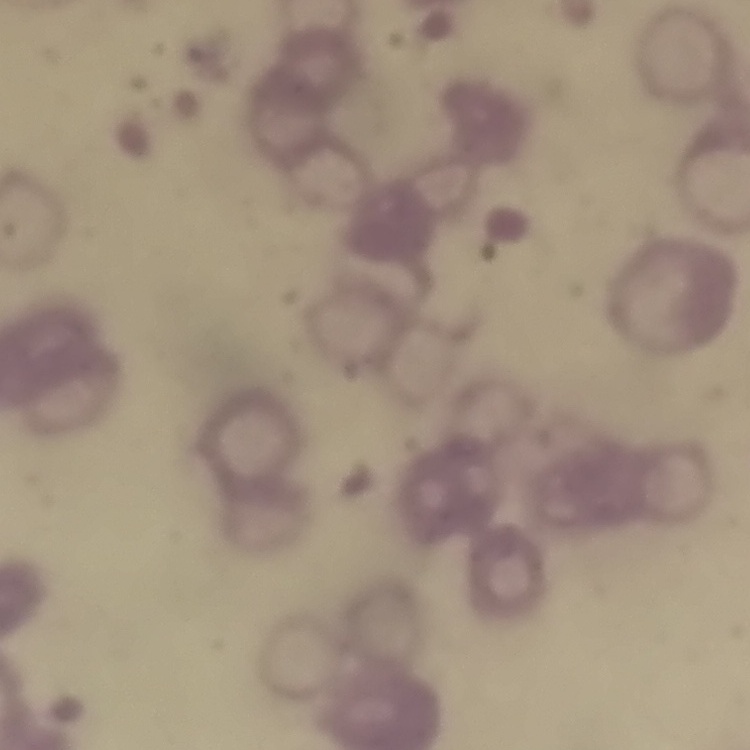
erythrocyte morphology = rouleaux formation
stain = Field's or Giemsa
image type = square crop of a larger photomicrograph
preparation = thin blood film